Name the parasite shown.
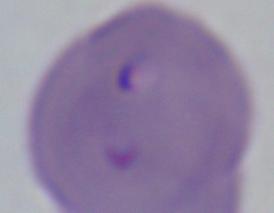

This is Babesia.

Photomicrograph. 1000x magnification.